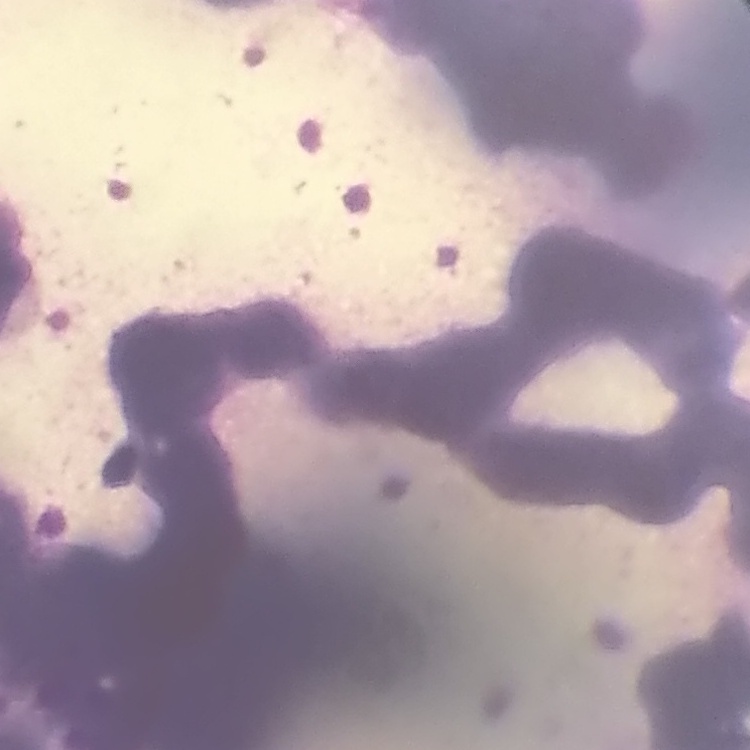
Summary:
  - Erythrocyte morphology: rouleaux formation
  - Stain: Field's or Giemsa
  - Image type: square crop of a larger photomicrograph
  - Preparation: thin peripheral smear